Describe the morphology of the erythrocytes.
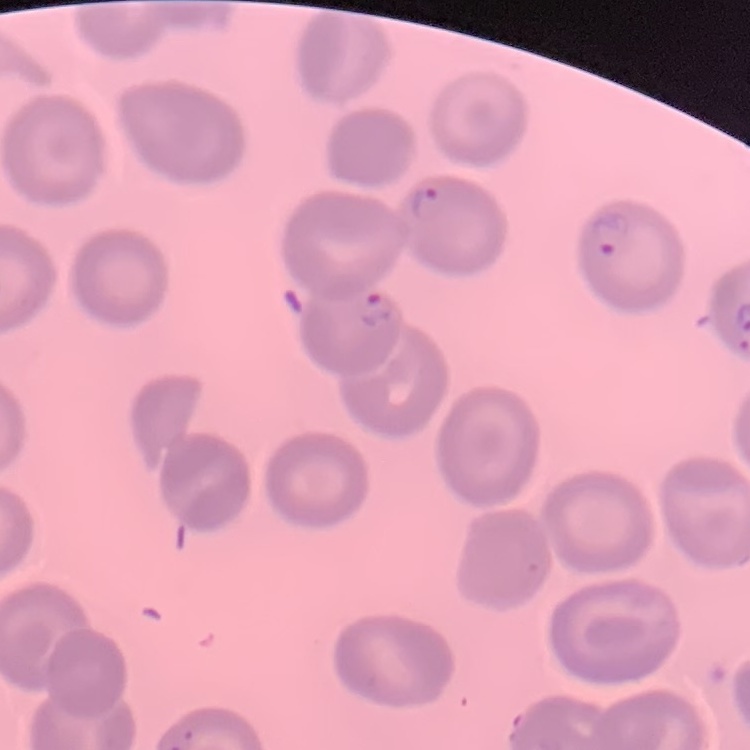
No rouleaux formation.

stain = Field's or Giemsa
image type = square crop of a larger photomicrograph
preparation = thin blood smear